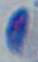

1000x magnification. Toxoplasma gondii is shown. Micrograph.